Give the position of every malaria parasite.
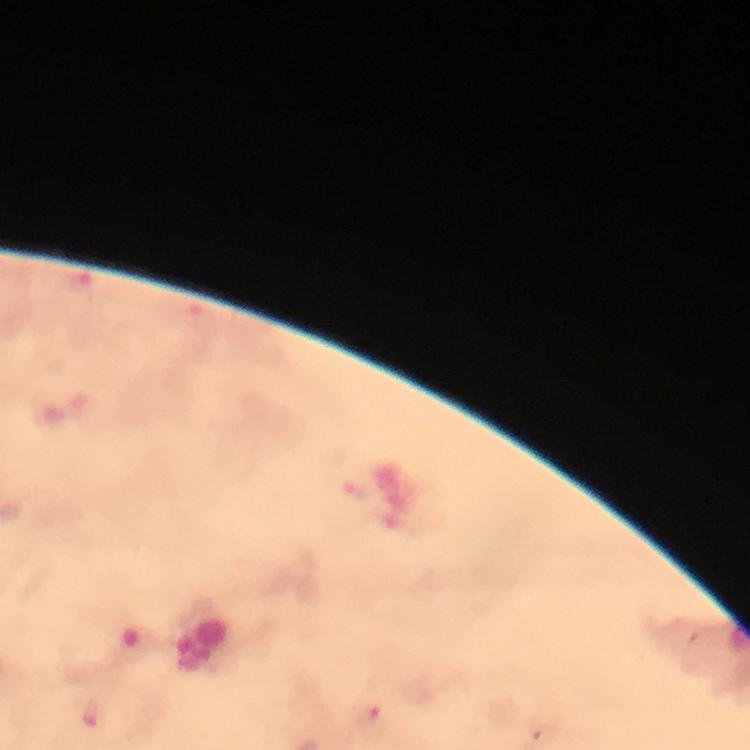
Approximate centers as {x, y} in pixels.
Malaria parasites: {80, 284}, {356, 491}, {371, 719}.

Summary:
  - Stain: Giemsa
  - Capture: smartphone mounted on the microscope
  - Magnification: 100x
  - Preparation: thick smear
  - Cropped from: a single field of view
  - Image size: 750×750 pixels
  - Context: from a malaria diagnostic workup
  - Immersion oil: applied